Locate every Plasmodium parasite.
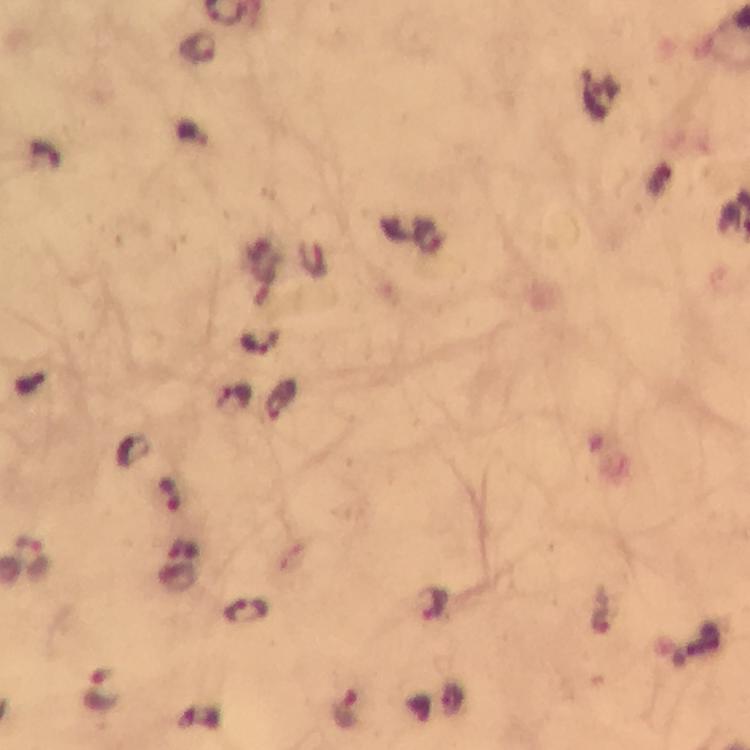
Approximate centers as [x, y] in pixels.
Plasmodium parasites: [197, 47], [259, 342], [281, 401], [171, 494], [34, 556], [432, 605], [248, 611], [100, 692], [348, 709].

Image is 750×750 pixels. Immersion oil was used. 100x magnification. From a malaria diagnostic workup. Giemsa stain. Thick blood film. A crop from one field of view. Photographed with a smartphone mounted on the microscope.